Report the malaria status of this cell.
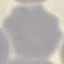

Uninfected.

stain = Giemsa
capture = smartphone camera at the microscope eyepiece
preparation = thin smear
image type = cell patch, automatically extracted from a larger field of view and resized to 64 × 64 pixels